State the blood parasite species.
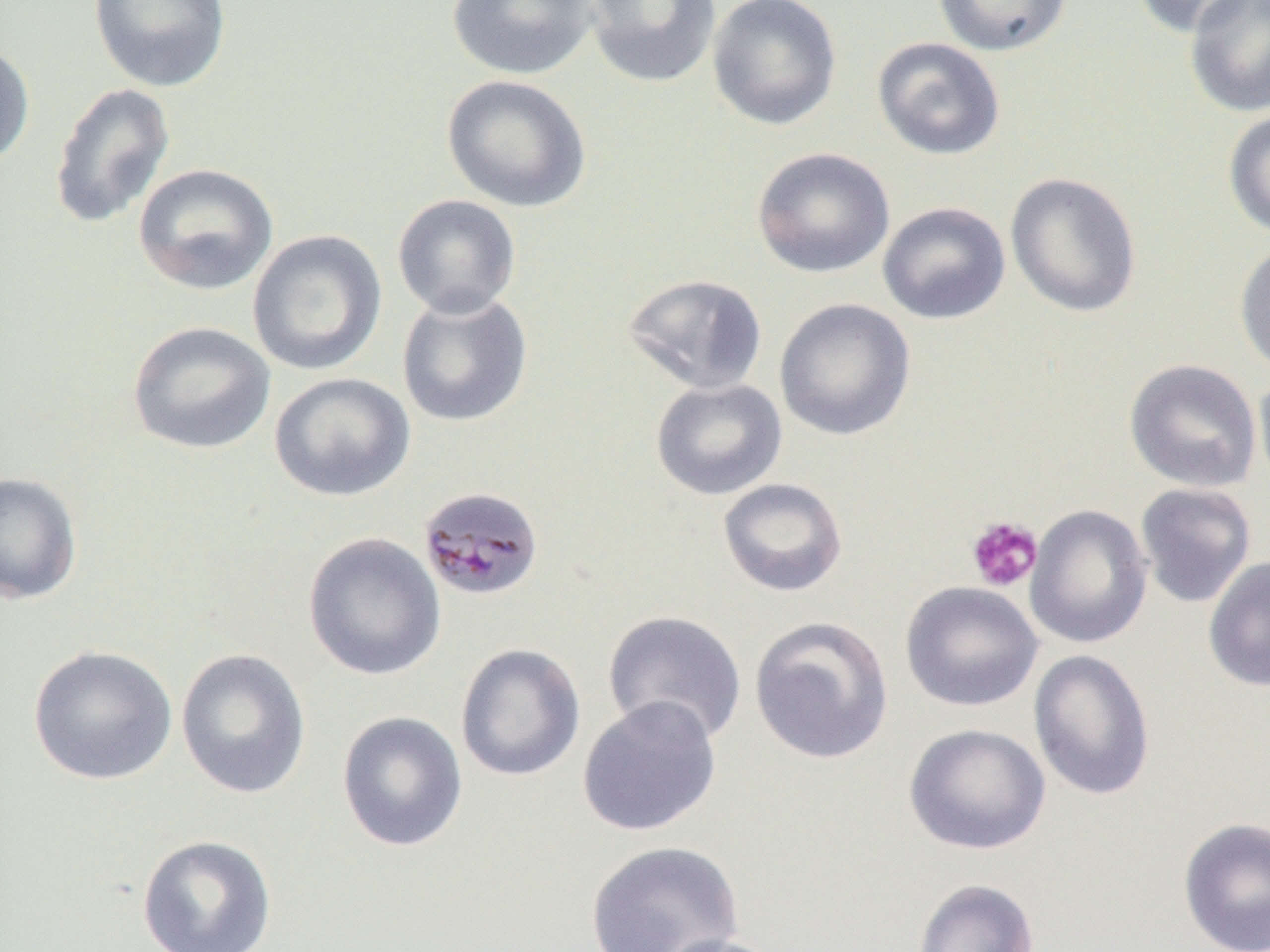

Plasmodium malariae.

magnification: 1000x
plasmodium_malariae_infected_red_blood_cell_locations: 'approximate bounding boxes as [x1, y1, x2, y2] in pixels: [426, 490, 544, 599]'
field_of_view: single
modality: optical microscopy
platelet_locations: 'approximate bounding boxes as [x1, y1, x2, y2] in pixels: [965, 515, 1042, 593]'
uninfected_red_blood_cell_locations: 'approximate bounding boxes as [x1, y1, x2, y2] in pixels: [88, 0, 231, 92], [446, 0, 601, 80], [583, 0, 721, 89], [706, 0, 843, 131], [932, 0, 1074, 57], [1130, 0, 1259, 38], [1183, 0, 1270, 118], [871, 36, 1006, 160], [0, 38, 35, 170], [441, 74, 592, 213], [49, 82, 176, 230], [1222, 107, 1270, 240], [751, 146, 895, 279], [132, 162, 279, 296], [1005, 171, 1143, 318], [391, 194, 522, 320], [877, 201, 1011, 325], [247, 229, 387, 377], [1234, 240, 1270, 377], [621, 274, 769, 395], [396, 290, 533, 428], [774, 298, 917, 441], [127, 321, 276, 455], [1124, 358, 1262, 493], [1253, 369, 1270, 498], [269, 371, 415, 502], [650, 378, 787, 500], [0, 470, 83, 605], [717, 477, 849, 598], [1134, 482, 1257, 609], [1025, 504, 1152, 648], [303, 532, 446, 680], [1203, 555, 1270, 692], [899, 581, 1043, 712], [602, 609, 747, 745], [749, 615, 894, 765], [455, 643, 586, 782], [27, 645, 178, 785], [176, 648, 312, 799], [1028, 649, 1156, 801], [576, 695, 722, 837], [336, 711, 468, 852], [903, 722, 1051, 855], [1177, 816, 1270, 952], [136, 834, 277, 951], [585, 839, 744, 952], [911, 878, 1040, 952], [652, 933, 788, 952]'
preparation: thin blood film
image_size: 1270×952 pixels